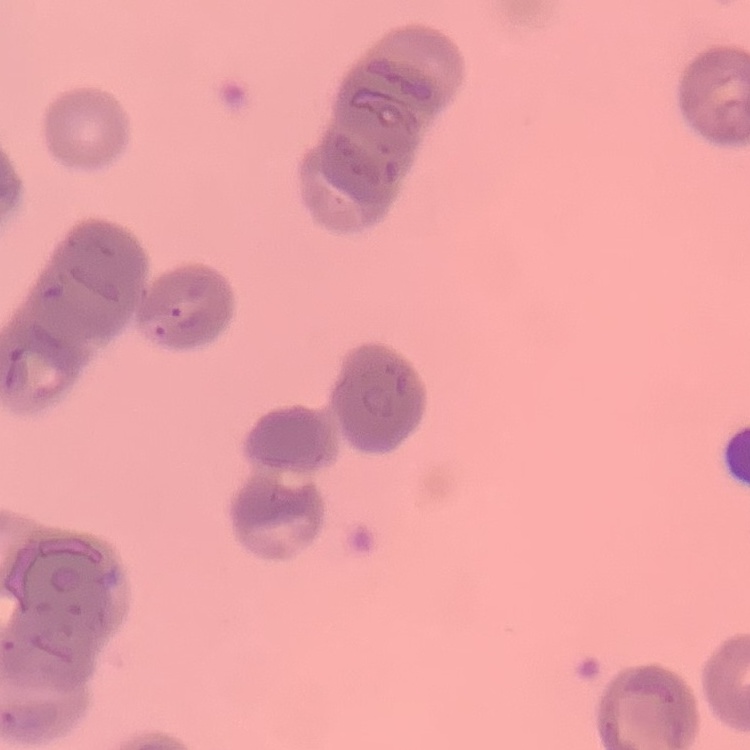 The red blood cells exhibit rouleaux formation. One tile cut from a larger photomicrograph. Field's or Giemsa stain. Thin peripheral smear.